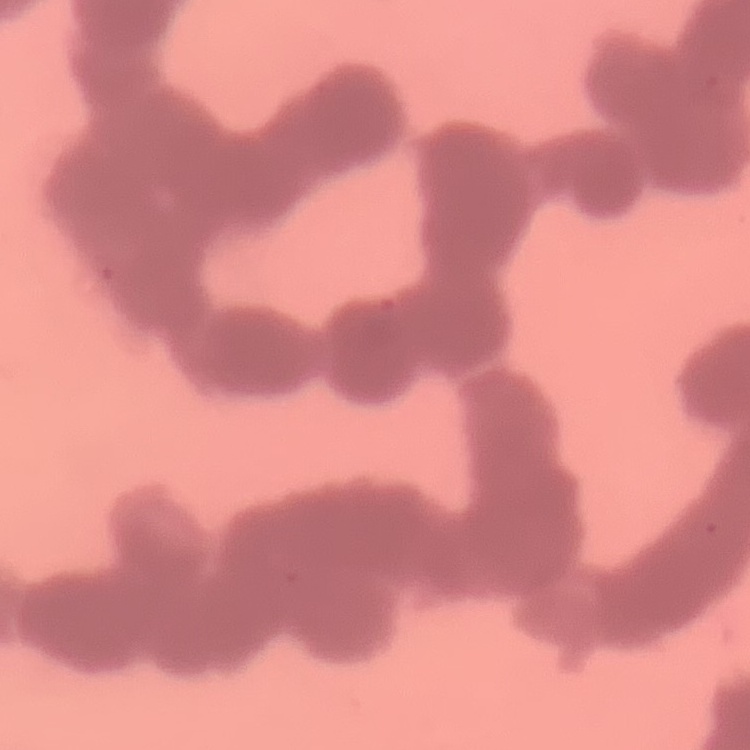
Summary:
  - Erythrocyte morphology: rouleaux formation
  - Stain: Field's or Giemsa
  - Preparation: thin peripheral smear
  - Image type: one tile cut from a larger photomicrograph